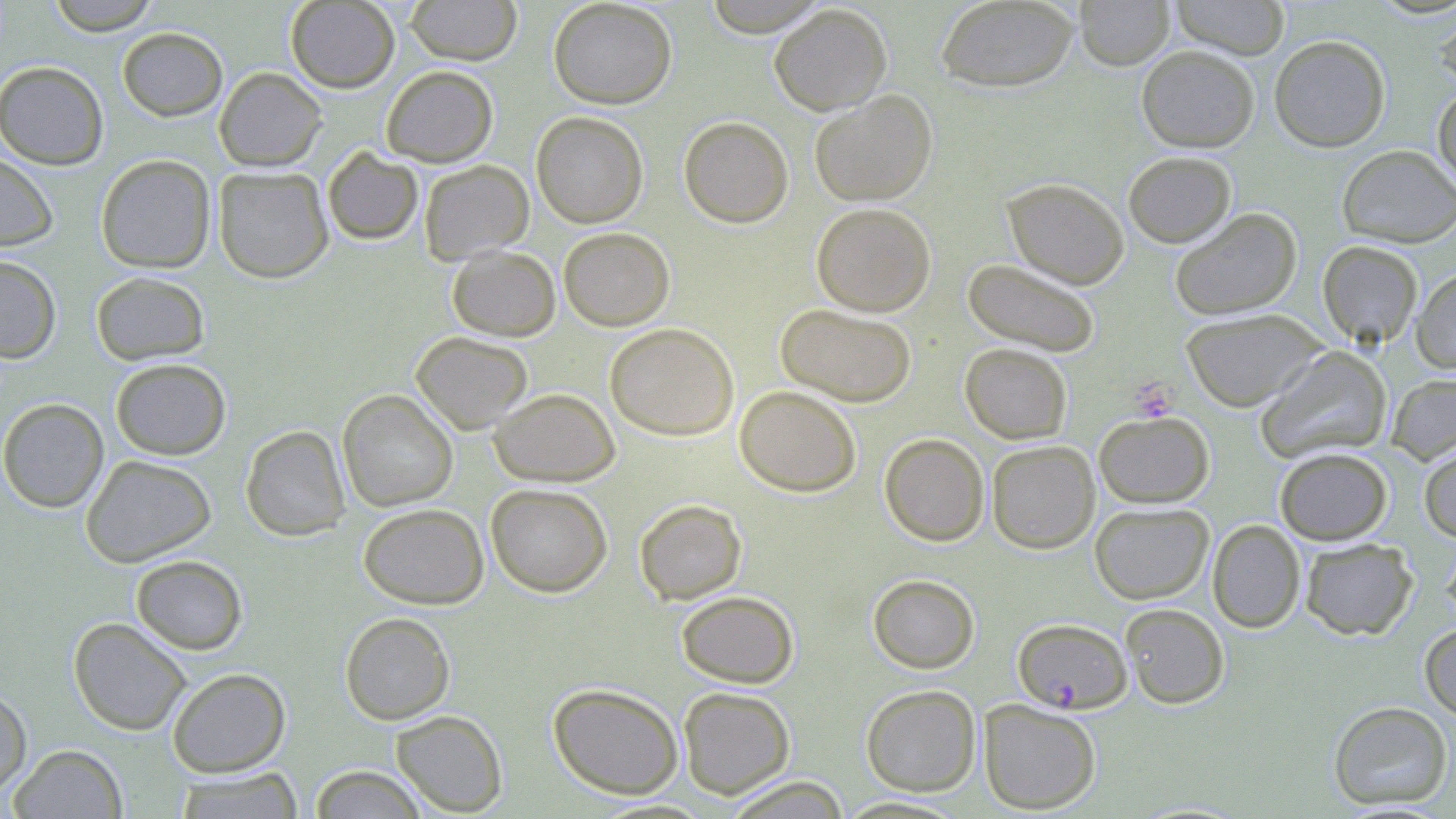
Approximate bounding boxes as named x1/y1/x2/y2 corners in pixels. Uninfected red blood cell locations: (x1=45, y1=0, x2=160, y2=35), (x1=405, y1=0, x2=521, y2=65), (x1=548, y1=0, x2=677, y2=109), (x1=700, y1=0, x2=831, y2=36), (x1=936, y1=0, x2=1078, y2=92), (x1=1075, y1=0, x2=1175, y2=70), (x1=1171, y1=0, x2=1290, y2=59), (x1=285, y1=1, x2=400, y2=93), (x1=769, y1=4, x2=892, y2=115), (x1=1433, y1=7, x2=1456, y2=96), (x1=117, y1=27, x2=228, y2=121), (x1=1269, y1=35, x2=1390, y2=152), (x1=1137, y1=45, x2=1259, y2=152), (x1=0, y1=61, x2=109, y2=169), (x1=381, y1=65, x2=498, y2=166), (x1=214, y1=67, x2=327, y2=171), (x1=1432, y1=86, x2=1456, y2=195), (x1=809, y1=90, x2=937, y2=207), (x1=532, y1=111, x2=648, y2=228), (x1=678, y1=115, x2=794, y2=228), (x1=1337, y1=145, x2=1456, y2=248), (x1=322, y1=147, x2=423, y2=245), (x1=1123, y1=151, x2=1236, y2=248), (x1=0, y1=152, x2=59, y2=251), (x1=95, y1=154, x2=216, y2=273), (x1=418, y1=160, x2=534, y2=264), (x1=213, y1=166, x2=334, y2=283), (x1=1002, y1=177, x2=1129, y2=289), (x1=811, y1=202, x2=936, y2=317), (x1=1170, y1=208, x2=1302, y2=320), (x1=558, y1=227, x2=675, y2=331), (x1=1317, y1=240, x2=1422, y2=347), (x1=446, y1=245, x2=560, y2=341), (x1=0, y1=254, x2=62, y2=363), (x1=963, y1=259, x2=1100, y2=356), (x1=1411, y1=267, x2=1456, y2=374), (x1=90, y1=271, x2=211, y2=365), (x1=775, y1=303, x2=917, y2=407), (x1=1180, y1=309, x2=1325, y2=411), (x1=604, y1=323, x2=739, y2=441), (x1=410, y1=331, x2=534, y2=434), (x1=960, y1=343, x2=1072, y2=444), (x1=1255, y1=346, x2=1391, y2=464), (x1=110, y1=357, x2=231, y2=460), (x1=1386, y1=373, x2=1456, y2=465), (x1=734, y1=385, x2=862, y2=497), (x1=488, y1=388, x2=620, y2=486), (x1=337, y1=389, x2=458, y2=512), (x1=0, y1=398, x2=109, y2=513), (x1=1094, y1=412, x2=1214, y2=508), (x1=240, y1=424, x2=351, y2=541), (x1=879, y1=433, x2=990, y2=546), (x1=987, y1=440, x2=1099, y2=554), (x1=1419, y1=444, x2=1456, y2=542), (x1=1275, y1=447, x2=1393, y2=545), (x1=80, y1=455, x2=216, y2=567), (x1=485, y1=483, x2=613, y2=597), (x1=634, y1=499, x2=747, y2=604), (x1=1089, y1=502, x2=1214, y2=604), (x1=357, y1=503, x2=489, y2=610), (x1=1207, y1=519, x2=1305, y2=633), (x1=1441, y1=535, x2=1456, y2=628), (x1=1300, y1=537, x2=1418, y2=640), (x1=130, y1=555, x2=248, y2=655), (x1=867, y1=573, x2=980, y2=673), (x1=676, y1=590, x2=799, y2=688), (x1=1120, y1=603, x2=1230, y2=709), (x1=339, y1=612, x2=455, y2=725), (x1=68, y1=617, x2=192, y2=735), (x1=1420, y1=622, x2=1456, y2=722), (x1=166, y1=667, x2=291, y2=777), (x1=547, y1=682, x2=684, y2=799), (x1=860, y1=684, x2=981, y2=796), (x1=0, y1=685, x2=32, y2=798), (x1=677, y1=686, x2=796, y2=799), (x1=979, y1=699, x2=1102, y2=815), (x1=1327, y1=700, x2=1454, y2=810), (x1=391, y1=710, x2=508, y2=816), (x1=9, y1=744, x2=127, y2=818), (x1=308, y1=764, x2=429, y2=818), (x1=173, y1=768, x2=304, y2=818), (x1=722, y1=776, x2=851, y2=818), (x1=832, y1=795, x2=971, y2=817). Plasmodium falciparum-infected red blood cell locations: (x1=1012, y1=618, x2=1132, y2=713). Platelet locations: (x1=1131, y1=377, x2=1179, y2=421). Slide-level diagnosis: Plasmodium falciparum. Image is 1456×819 pixels. May-Grünwald-Giemsa-stained preparation. One field of a larger specimen. Thin blood film. 1000x magnification. Light microscopy.